Report the malaria status of this cell.
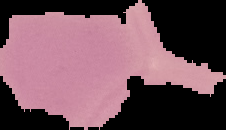
It is uninfected.

Segmented cell region on a black background. Image is 226×130 pixels. From a thin blood smear.